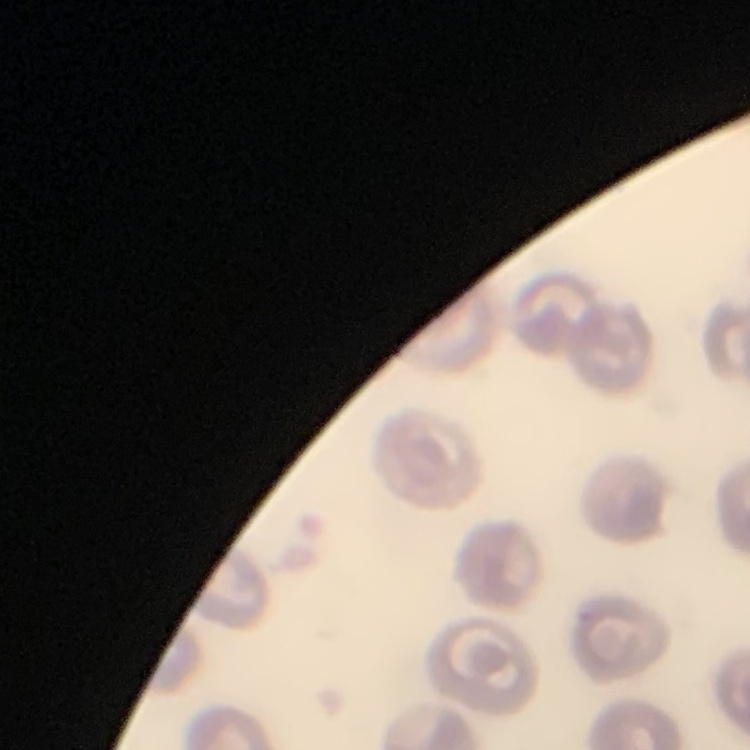
Summary:
  - Red blood cell morphology: no rouleaux formation
  - Stain: Field's or Giemsa
  - Preparation: thin blood film
  - Image type: one tile cut from a larger photomicrograph